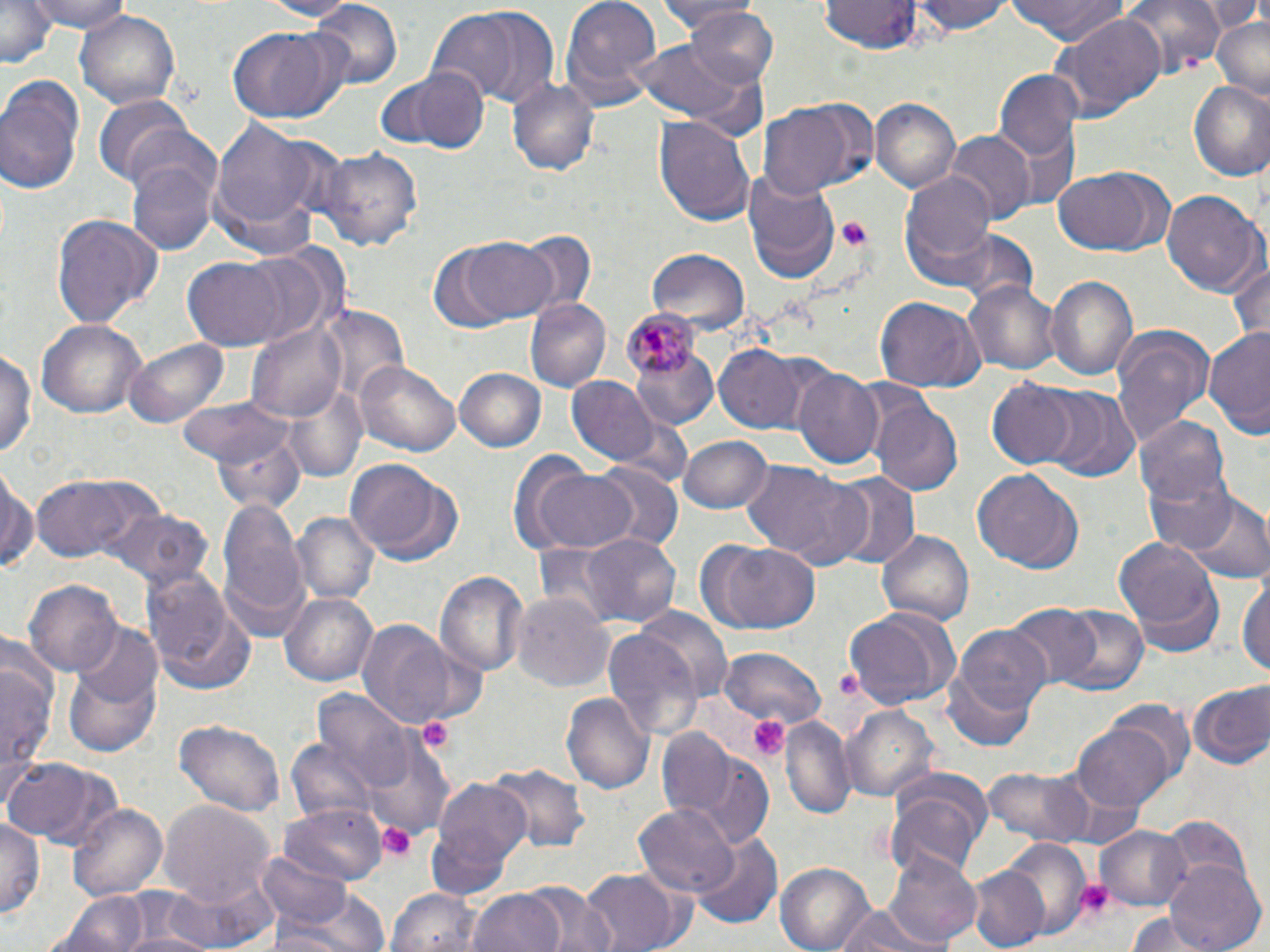
Summary:
  - Coordinate format: approximate bounding boxes as named x1/y1/x2/y2 corners in pixels
  - Platelet locations: (x1=834, y1=216, x2=872, y2=253), (x1=827, y1=667, x2=870, y2=707), (x1=748, y1=715, x2=789, y2=762), (x1=416, y1=716, x2=456, y2=754), (x1=378, y1=822, x2=417, y2=862), (x1=1074, y1=877, x2=1116, y2=921)
  - Plasmodium malariae-infected red blood cell locations: (x1=623, y1=310, x2=701, y2=379)
  - Uninfected red blood cell locations: (x1=2, y1=0, x2=57, y2=67), (x1=30, y1=0, x2=131, y2=35), (x1=253, y1=0, x2=360, y2=20), (x1=559, y1=0, x2=662, y2=111), (x1=650, y1=0, x2=761, y2=29), (x1=820, y1=0, x2=925, y2=56), (x1=915, y1=0, x2=1011, y2=37), (x1=1007, y1=0, x2=1136, y2=46), (x1=1115, y1=0, x2=1226, y2=83), (x1=1201, y1=0, x2=1266, y2=36), (x1=310, y1=2, x2=405, y2=87), (x1=74, y1=7, x2=182, y2=111), (x1=441, y1=7, x2=562, y2=107), (x1=679, y1=8, x2=780, y2=88), (x1=1049, y1=13, x2=1166, y2=123), (x1=1209, y1=15, x2=1269, y2=100), (x1=228, y1=28, x2=343, y2=120), (x1=633, y1=37, x2=753, y2=125), (x1=395, y1=68, x2=490, y2=151), (x1=994, y1=70, x2=1084, y2=170), (x1=0, y1=74, x2=87, y2=198), (x1=507, y1=76, x2=599, y2=177), (x1=1187, y1=81, x2=1270, y2=179), (x1=94, y1=95, x2=197, y2=186), (x1=869, y1=97, x2=960, y2=194), (x1=757, y1=106, x2=856, y2=199), (x1=654, y1=113, x2=755, y2=229), (x1=207, y1=118, x2=326, y2=244), (x1=946, y1=130, x2=1033, y2=224), (x1=319, y1=145, x2=425, y2=255), (x1=126, y1=151, x2=218, y2=257), (x1=741, y1=167, x2=837, y2=284), (x1=900, y1=168, x2=998, y2=278), (x1=1053, y1=169, x2=1170, y2=257), (x1=1161, y1=189, x2=1265, y2=297), (x1=49, y1=214, x2=162, y2=328), (x1=919, y1=227, x2=1042, y2=309), (x1=516, y1=230, x2=603, y2=317), (x1=454, y1=236, x2=561, y2=322), (x1=239, y1=247, x2=340, y2=348), (x1=646, y1=249, x2=749, y2=333), (x1=1224, y1=251, x2=1270, y2=346), (x1=185, y1=257, x2=289, y2=349), (x1=1045, y1=272, x2=1139, y2=386), (x1=964, y1=279, x2=1061, y2=377), (x1=874, y1=295, x2=986, y2=392), (x1=524, y1=298, x2=610, y2=394), (x1=35, y1=320, x2=145, y2=419), (x1=249, y1=321, x2=348, y2=422), (x1=1111, y1=325, x2=1216, y2=450), (x1=1203, y1=328, x2=1270, y2=431), (x1=127, y1=338, x2=230, y2=429), (x1=0, y1=344, x2=37, y2=461), (x1=630, y1=344, x2=720, y2=431), (x1=714, y1=344, x2=809, y2=434), (x1=354, y1=357, x2=461, y2=460), (x1=453, y1=368, x2=546, y2=452), (x1=793, y1=368, x2=884, y2=467), (x1=566, y1=378, x2=661, y2=467), (x1=987, y1=380, x2=1080, y2=468), (x1=1039, y1=387, x2=1138, y2=480), (x1=291, y1=390, x2=375, y2=481), (x1=177, y1=396, x2=299, y2=466), (x1=870, y1=398, x2=962, y2=494), (x1=1135, y1=414, x2=1231, y2=510), (x1=212, y1=427, x2=308, y2=510), (x1=678, y1=435, x2=772, y2=513), (x1=520, y1=459, x2=641, y2=556), (x1=345, y1=460, x2=462, y2=566), (x1=742, y1=461, x2=859, y2=565), (x1=0, y1=462, x2=39, y2=578), (x1=594, y1=462, x2=683, y2=551), (x1=971, y1=468, x2=1081, y2=574), (x1=1144, y1=468, x2=1241, y2=556), (x1=825, y1=472, x2=921, y2=569), (x1=32, y1=473, x2=155, y2=563), (x1=1179, y1=489, x2=1270, y2=587), (x1=217, y1=496, x2=307, y2=635), (x1=100, y1=507, x2=209, y2=594), (x1=292, y1=513, x2=380, y2=606), (x1=876, y1=528, x2=973, y2=625), (x1=579, y1=531, x2=682, y2=631), (x1=1115, y1=533, x2=1223, y2=647), (x1=698, y1=540, x2=820, y2=634), (x1=142, y1=567, x2=252, y2=691), (x1=435, y1=569, x2=528, y2=677), (x1=1238, y1=570, x2=1270, y2=683), (x1=24, y1=580, x2=124, y2=675), (x1=280, y1=592, x2=379, y2=687), (x1=514, y1=593, x2=615, y2=694), (x1=841, y1=604, x2=959, y2=709), (x1=1005, y1=604, x2=1103, y2=691), (x1=1053, y1=605, x2=1147, y2=698), (x1=631, y1=611, x2=730, y2=712), (x1=354, y1=621, x2=474, y2=731), (x1=944, y1=622, x2=1050, y2=751), (x1=74, y1=623, x2=164, y2=707), (x1=600, y1=630, x2=703, y2=741), (x1=720, y1=646, x2=824, y2=725), (x1=0, y1=647, x2=57, y2=798), (x1=63, y1=657, x2=162, y2=757), (x1=1186, y1=681, x2=1269, y2=771), (x1=312, y1=690, x2=412, y2=792), (x1=561, y1=692, x2=654, y2=796), (x1=1101, y1=699, x2=1195, y2=788), (x1=843, y1=706, x2=939, y2=804), (x1=780, y1=716, x2=856, y2=822), (x1=176, y1=718, x2=284, y2=820), (x1=1073, y1=722, x2=1175, y2=814), (x1=653, y1=728, x2=743, y2=820), (x1=364, y1=735, x2=453, y2=839), (x1=287, y1=742, x2=384, y2=844), (x1=672, y1=743, x2=776, y2=848), (x1=2, y1=757, x2=119, y2=848), (x1=487, y1=764, x2=592, y2=852), (x1=983, y1=764, x2=1098, y2=846), (x1=430, y1=776, x2=533, y2=884), (x1=886, y1=780, x2=991, y2=880), (x1=159, y1=802, x2=274, y2=911), (x1=69, y1=803, x2=167, y2=905), (x1=631, y1=803, x2=739, y2=894), (x1=281, y1=805, x2=385, y2=883), (x1=0, y1=818, x2=43, y2=922), (x1=1159, y1=818, x2=1260, y2=919), (x1=1095, y1=824, x2=1193, y2=911), (x1=691, y1=833, x2=781, y2=929), (x1=999, y1=837, x2=1091, y2=938), (x1=883, y1=848, x2=980, y2=950), (x1=1162, y1=859, x2=1266, y2=952), (x1=778, y1=860, x2=877, y2=952), (x1=256, y1=864, x2=387, y2=952), (x1=965, y1=864, x2=1050, y2=952), (x1=580, y1=867, x2=682, y2=951), (x1=171, y1=874, x2=280, y2=949), (x1=522, y1=884, x2=614, y2=952), (x1=385, y1=887, x2=484, y2=952), (x1=467, y1=888, x2=570, y2=952), (x1=57, y1=891, x2=149, y2=952), (x1=829, y1=904, x2=939, y2=952), (x1=1127, y1=914, x2=1217, y2=952)
  - Slide-level diagnosis: Plasmodium malariae
  - Image size: 1270×952 pixels
  - Modality: light microscopy
  - Stain: May-Grünwald-Giemsa
  - Preparation: thin blood film
  - Magnification: 1000x
  - Field of view: one of a larger specimen